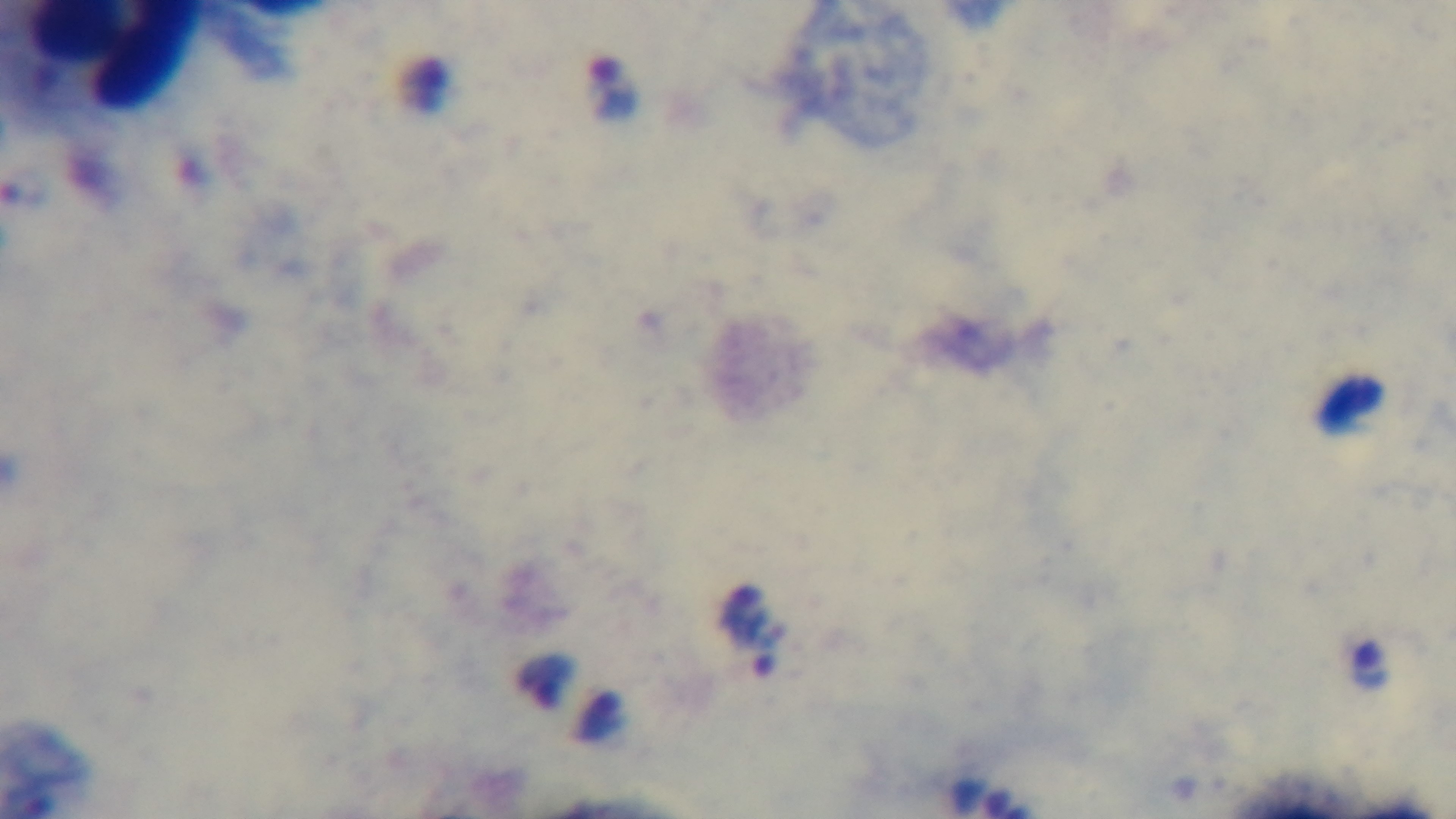

objective = 100x oil immersion
capture = mounted 4K digital camera
malaria status = positive
field of view = one from the slide
preparation = thick
modality = light microscopy
stain = Giemsa